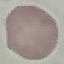

Result: no malaria parasites detected. Cell patch, automatically extracted from a larger field of view and resized to 64 × 64 pixels. Giemsa-stained preparation. Photographed with a smartphone camera at the microscope eyepiece. Thin blood film.